Name the parasite shown.
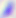

This is Toxoplasma gondii.

modality = micrograph
magnification = 400x